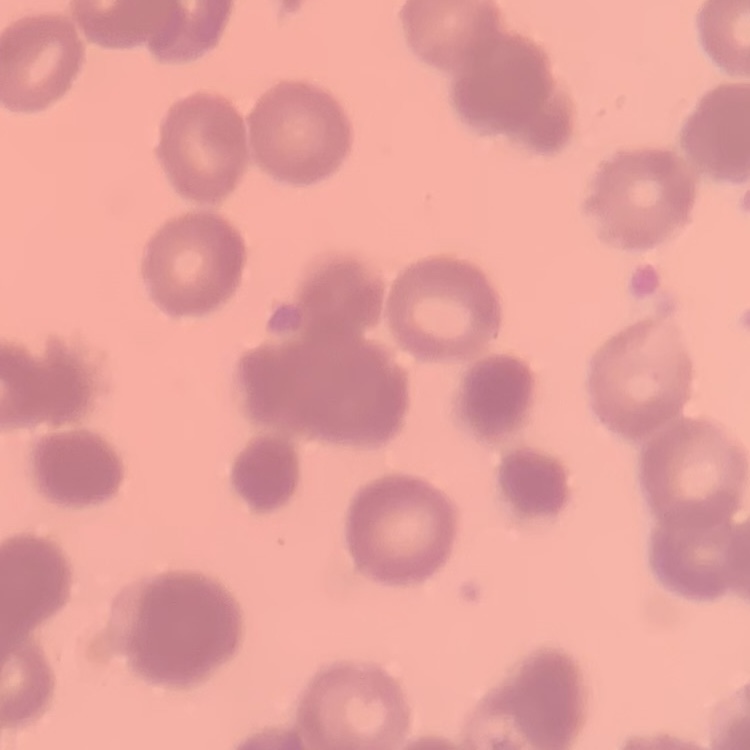

Summary:
  - Red blood cell morphology: rouleaux formation
  - Stain: Field's or Giemsa
  - Preparation: thin blood smear
  - Image type: square crop of a larger photomicrograph